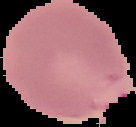
{
  "preparation": "thin blood smear",
  "image_type": "segmented cell region with the area outside set to black",
  "malaria_status": "parasitized",
  "image_size": "136×127 pixels"
}